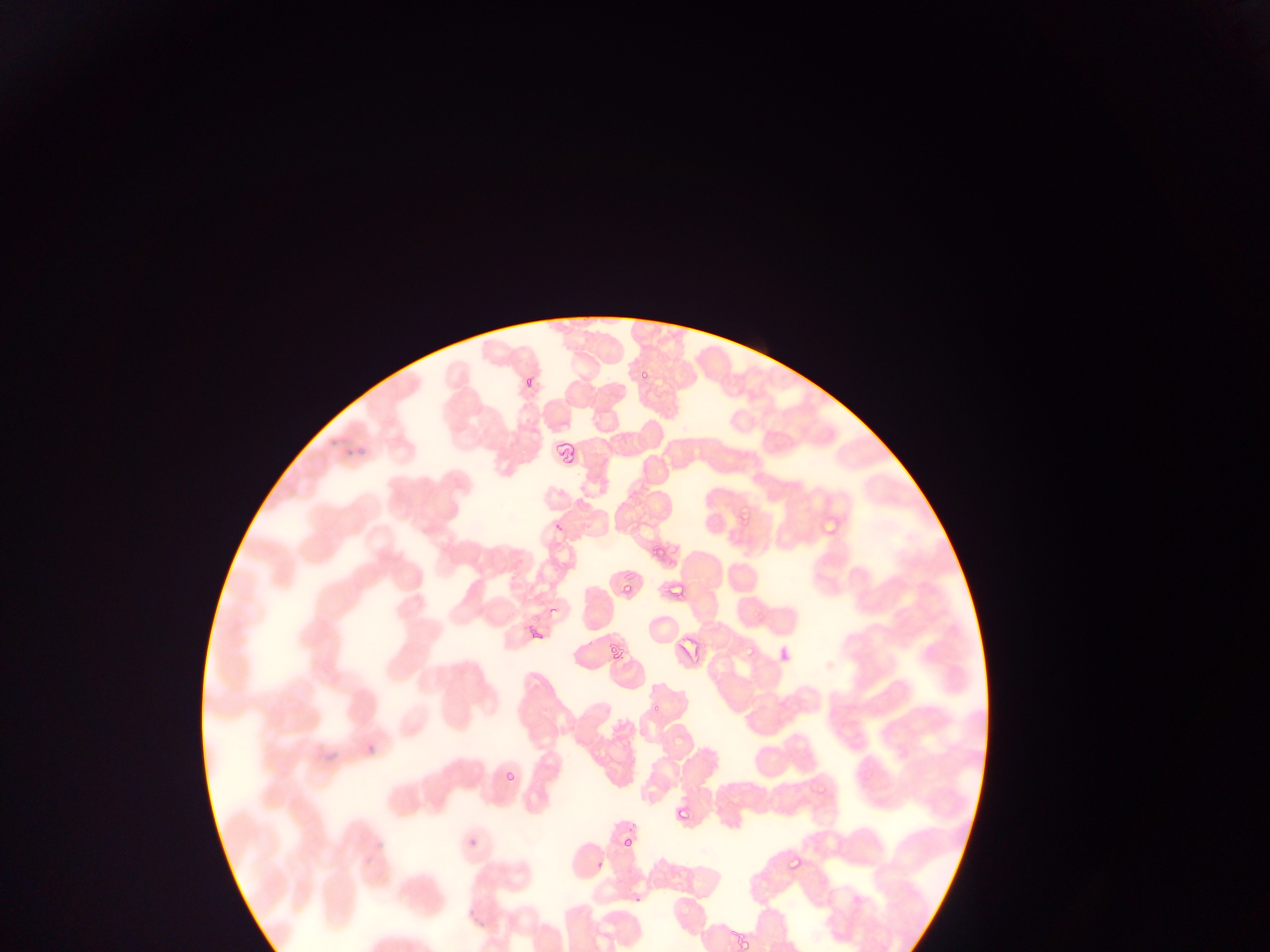
Approximate bounding boxes as [left, top, right, bottom] in pixels.
Summary:
  - Plasmodium parasite locations: [637, 362, 651, 382], [522, 367, 535, 384], [740, 504, 753, 526], [648, 542, 658, 556], [623, 579, 635, 596], [606, 642, 626, 665], [744, 642, 755, 658], [652, 698, 665, 715], [505, 765, 517, 783], [673, 804, 694, 827], [623, 836, 633, 849], [786, 857, 804, 871] | approximate [x, y] pixel centers of objects too small to bound: [633, 826]
  - Leukocyte locations: [371, 923, 418, 952]
  - Preparation: thin blood film
  - Field of view: single
  - Capture: mobile-phone photograph through a microscope
  - Country: Ghana
  - Image size: 1270×952 pixels